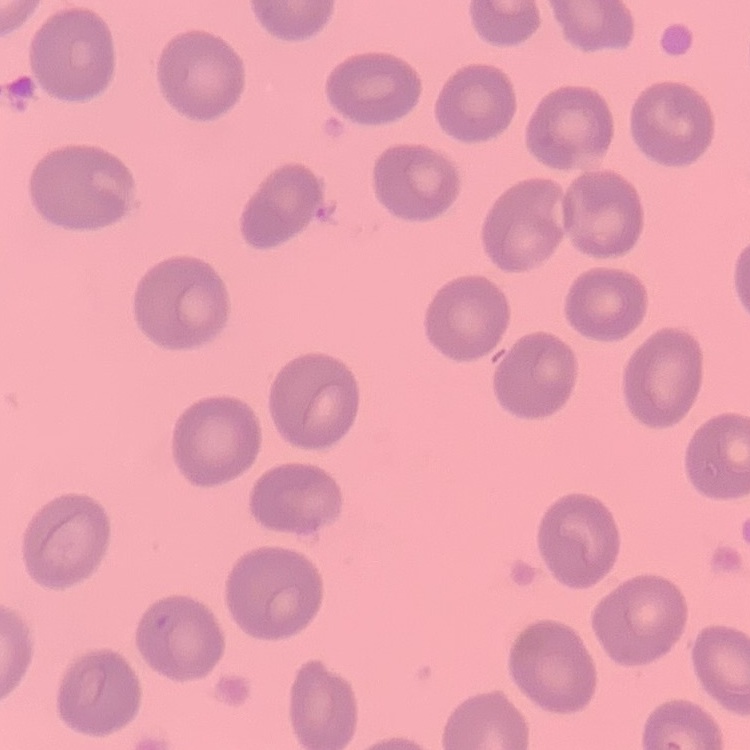 The erythrocytes exhibit no rouleaux formation. Stained with either Field's or Giemsa. Thin blood smear. One tile cut from a larger photomicrograph.